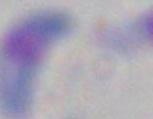

Toxoplasma gondii is shown. Captured at 1000x magnification. Micrograph.